Identify the cell.
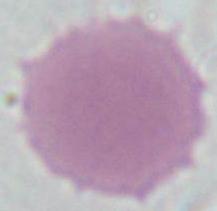

An erythrocyte.

modality: photomicrograph
magnification: 1000x